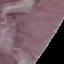

malaria status = uninfected
stain = Giemsa
image type = cell patch, automatically extracted from a larger field of view and resized to 64 × 64 pixels
preparation = thin blood smear
capture = smartphone camera at the microscope eyepiece